Identify the parasite.
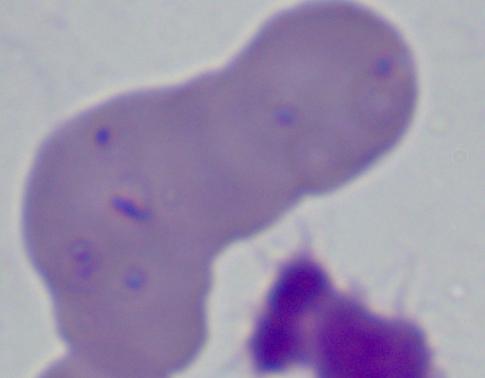
This is Babesia.

Summary:
  - Magnification: 1000x
  - Modality: micrograph